Describe the morphology of the red blood cells.
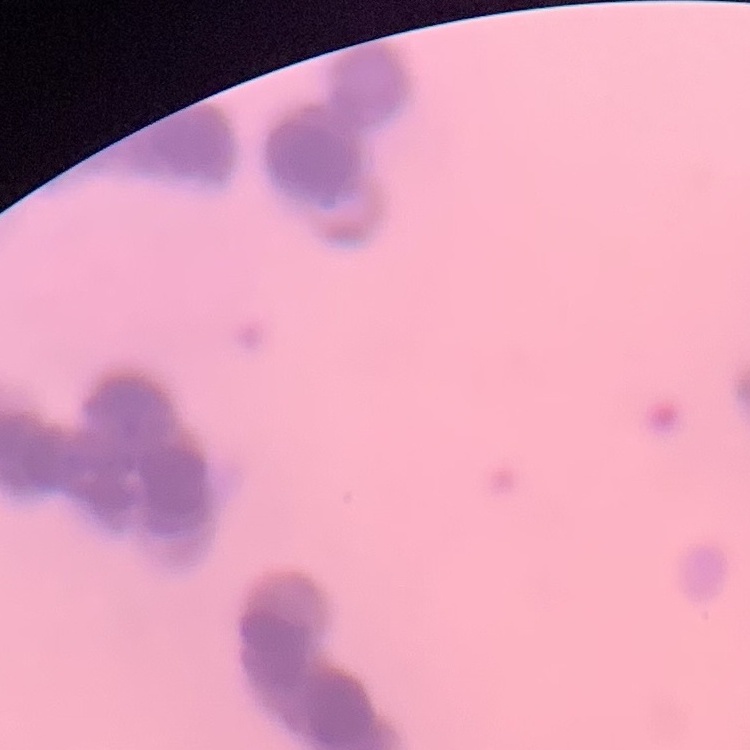

They show rouleaux formation.

stain = Field's or Giemsa
image type = square crop of a larger photomicrograph
preparation = thin peripheral smear